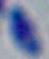
modality = photomicrograph
magnification = 1000x
identification = Toxoplasma gondii